Point out each malaria parasite.
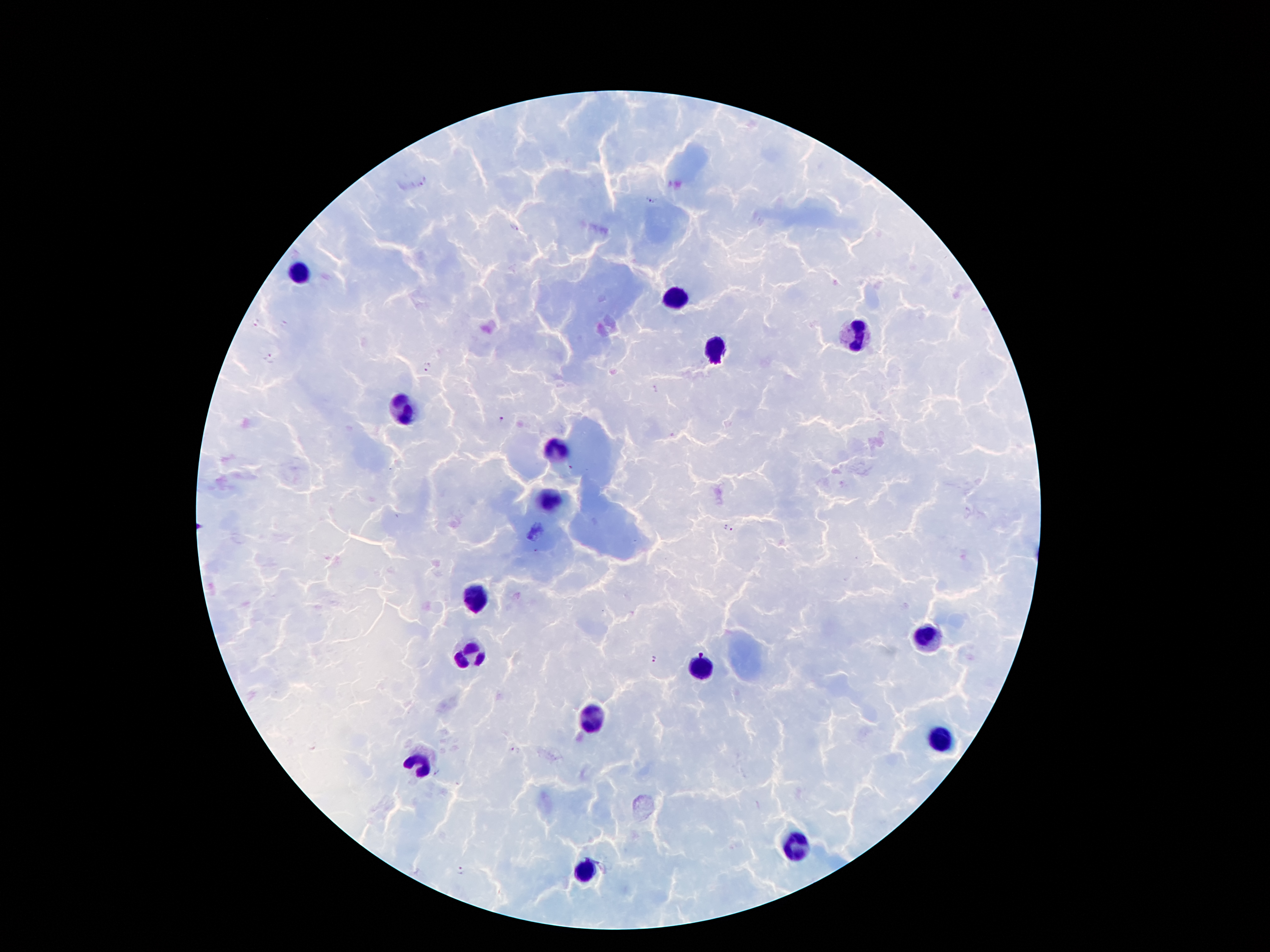

Approximate centers as [x, y] in pixels.
Malaria parasites: [423, 183], [652, 202], [512, 228], [258, 322], [268, 359], [427, 366], [654, 388], [502, 420], [569, 467], [724, 527], [732, 530], [654, 660], [515, 752], [437, 773], [459, 871].

image_size: 1270×952 pixels
stain: Giemsa
field_of_view: one from this slide
patient_malaria_status: positive for Plasmodium falciparum
leukocyte_locations: 'approximate centers as [x, y] in pixels: [297, 273], [678, 296], [857, 332], [717, 350], [401, 409], [556, 452], [555, 502], [478, 597], [926, 636], [467, 654], [699, 670], [594, 720], [942, 736], [417, 761], [799, 841], [587, 870]'
magnification: 100x
preparation: thick blood smear
capture: smartphone through the microscope eyepiece